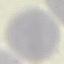

Summary:
  - Malaria status: uninfected
  - Image type: cell patch, automatically extracted from a larger field of view and resized to 64 × 64 pixels
  - Stain: Giemsa
  - Preparation: thin smear
  - Capture: smartphone camera at the microscope eyepiece